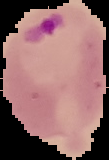
Malaria status: parasitized. From a thin blood film. Image is 109×160 pixels. Segmented cell region on a black background.